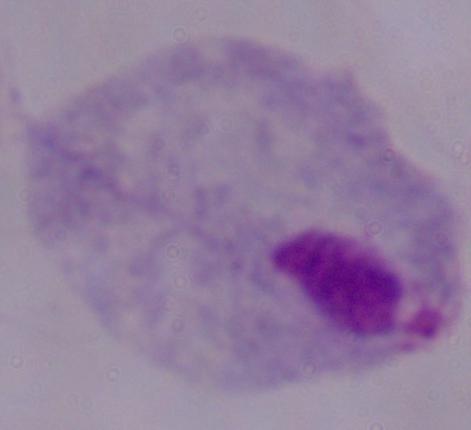
identification: trichomonad
magnification: 1000x
modality: photomicrograph